Identify the blood parasite species.
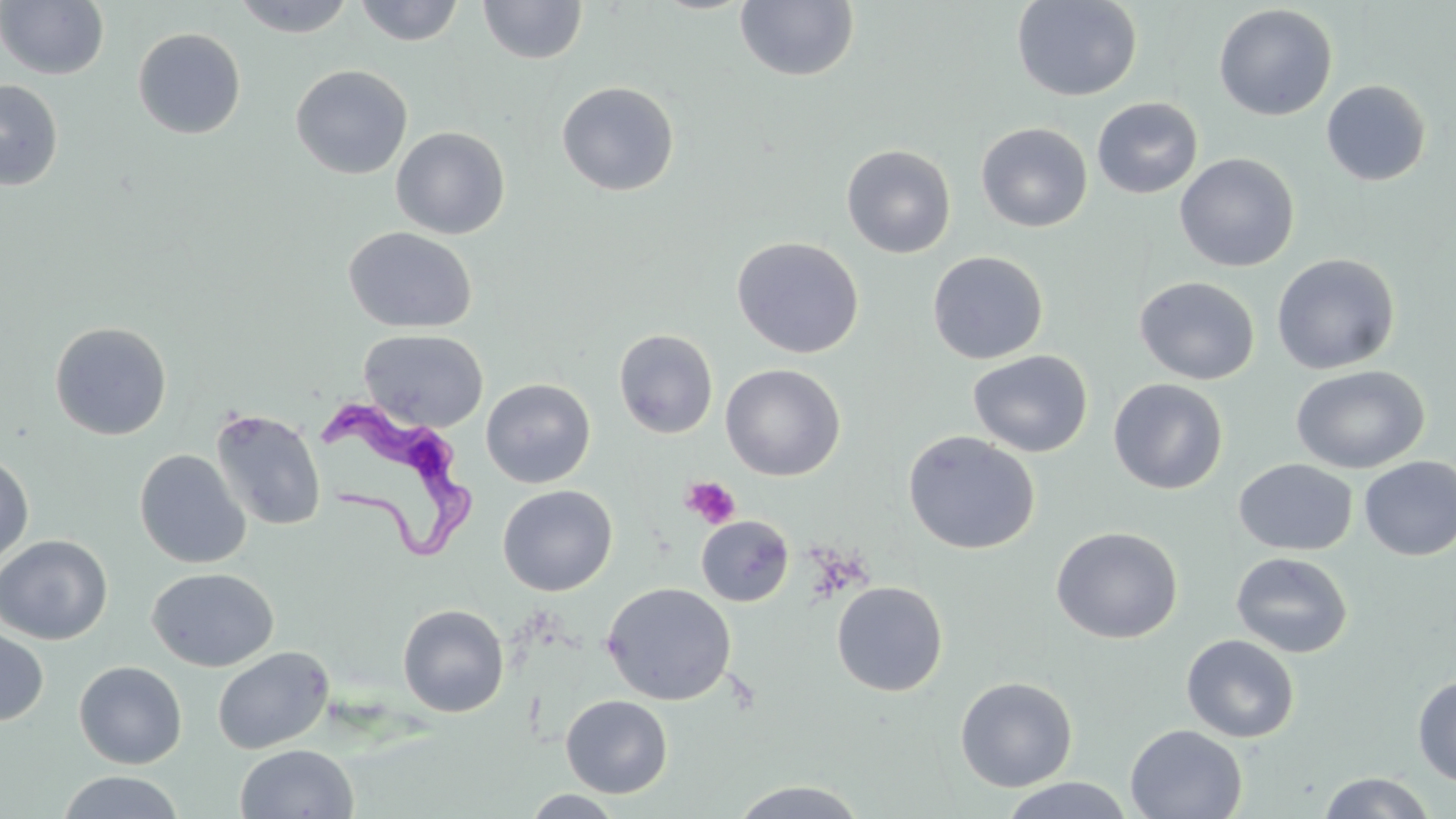
Trypanosoma brucei.

Approximate bounding boxes as named x1/y1/x2/y2 corners in pixels. Trypanosoma brucei locations: (x1=308, y1=393, x2=479, y2=564). Uninfected red blood cell locations: (x1=231, y1=0, x2=356, y2=38), (x1=354, y1=0, x2=466, y2=46), (x1=1011, y1=0, x2=1143, y2=102), (x1=0, y1=1, x2=109, y2=80), (x1=478, y1=1, x2=588, y2=65), (x1=735, y1=1, x2=859, y2=82), (x1=1213, y1=4, x2=1337, y2=121), (x1=132, y1=28, x2=246, y2=139), (x1=290, y1=64, x2=412, y2=179), (x1=0, y1=79, x2=64, y2=191), (x1=1321, y1=80, x2=1432, y2=186), (x1=556, y1=81, x2=679, y2=196), (x1=1092, y1=96, x2=1203, y2=199), (x1=976, y1=122, x2=1093, y2=232), (x1=390, y1=127, x2=511, y2=239), (x1=841, y1=144, x2=957, y2=258), (x1=1174, y1=152, x2=1299, y2=272), (x1=344, y1=226, x2=477, y2=334), (x1=730, y1=236, x2=865, y2=359), (x1=927, y1=251, x2=1049, y2=365), (x1=1271, y1=253, x2=1401, y2=375), (x1=1134, y1=276, x2=1260, y2=385), (x1=49, y1=321, x2=172, y2=440), (x1=613, y1=328, x2=719, y2=438), (x1=359, y1=329, x2=489, y2=432), (x1=967, y1=350, x2=1093, y2=458), (x1=720, y1=363, x2=846, y2=481), (x1=1290, y1=365, x2=1430, y2=474), (x1=480, y1=378, x2=596, y2=488), (x1=1108, y1=378, x2=1229, y2=494), (x1=209, y1=408, x2=327, y2=532), (x1=903, y1=430, x2=1041, y2=555), (x1=134, y1=449, x2=251, y2=569), (x1=0, y1=450, x2=35, y2=567), (x1=1359, y1=456, x2=1456, y2=560), (x1=1233, y1=458, x2=1357, y2=555), (x1=498, y1=484, x2=617, y2=596), (x1=696, y1=515, x2=794, y2=606), (x1=1050, y1=526, x2=1183, y2=644), (x1=0, y1=534, x2=112, y2=645), (x1=1230, y1=551, x2=1353, y2=658), (x1=147, y1=567, x2=279, y2=672), (x1=831, y1=581, x2=948, y2=697), (x1=601, y1=582, x2=737, y2=705), (x1=398, y1=604, x2=509, y2=717), (x1=0, y1=627, x2=49, y2=727), (x1=1181, y1=634, x2=1300, y2=743), (x1=212, y1=647, x2=334, y2=754), (x1=74, y1=661, x2=188, y2=769), (x1=1412, y1=674, x2=1456, y2=786), (x1=955, y1=676, x2=1078, y2=792), (x1=561, y1=694, x2=673, y2=798), (x1=1124, y1=724, x2=1248, y2=819), (x1=234, y1=744, x2=359, y2=819), (x1=57, y1=771, x2=185, y2=819), (x1=1316, y1=772, x2=1438, y2=818), (x1=998, y1=776, x2=1136, y2=819), (x1=727, y1=780, x2=870, y2=818), (x1=522, y1=790, x2=626, y2=818). Platelet locations: (x1=681, y1=475, x2=741, y2=529). Image is 1456×819 pixels. Captured at 1000x magnification. May-Grünwald-Giemsa stain. Single field of view. Thin blood film. Light microscopy.